Outline each Plasmodium falciparum-infected red blood cell.
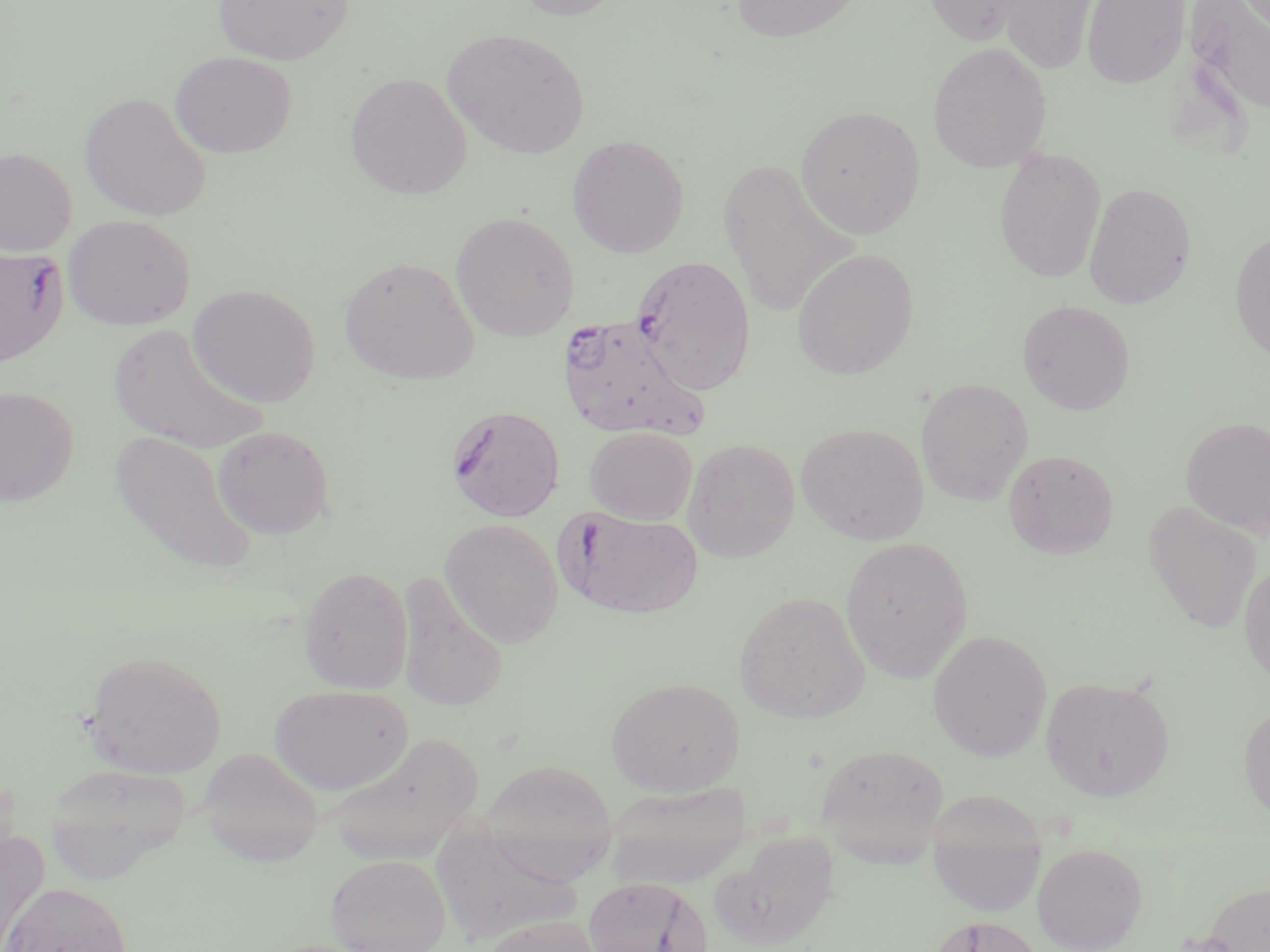

Approximate bounding boxes as named x1/y1/x2/y2 corners in pixels.
Plasmodium falciparum-infected red blood cells: (x1=0, y1=245, x2=68, y2=366), (x1=632, y1=254, x2=756, y2=395), (x1=558, y1=313, x2=710, y2=441), (x1=447, y1=404, x2=566, y2=522), (x1=558, y1=509, x2=705, y2=619).

slide-level diagnosis = Plasmodium falciparum
magnification = 1000x
modality = optical microscopy
stain = May-Grünwald-Giemsa
field of view = single
image size = 1270×952 pixels
preparation = thin blood film
uninfected red blood cell locations = approximate bounding boxes as named x1/y1/x2/y2 corners in pixels: (x1=213, y1=0, x2=354, y2=65), (x1=510, y1=0, x2=627, y2=20), (x1=730, y1=0, x2=861, y2=43), (x1=924, y1=0, x2=1029, y2=46), (x1=1082, y1=0, x2=1191, y2=89), (x1=1182, y1=0, x2=1270, y2=120), (x1=998, y1=1, x2=1099, y2=74), (x1=442, y1=28, x2=590, y2=159), (x1=927, y1=42, x2=1052, y2=173), (x1=169, y1=51, x2=297, y2=158), (x1=345, y1=72, x2=472, y2=199), (x1=79, y1=91, x2=213, y2=222), (x1=795, y1=105, x2=925, y2=239), (x1=567, y1=135, x2=689, y2=258), (x1=0, y1=147, x2=77, y2=256), (x1=994, y1=148, x2=1106, y2=283), (x1=718, y1=156, x2=857, y2=320), (x1=1083, y1=182, x2=1197, y2=309), (x1=450, y1=211, x2=580, y2=342), (x1=63, y1=215, x2=195, y2=330), (x1=1230, y1=229, x2=1270, y2=362), (x1=791, y1=247, x2=919, y2=379), (x1=339, y1=255, x2=480, y2=385), (x1=188, y1=284, x2=321, y2=408), (x1=1017, y1=300, x2=1135, y2=415), (x1=107, y1=323, x2=269, y2=456), (x1=915, y1=377, x2=1034, y2=506), (x1=0, y1=386, x2=79, y2=507), (x1=1181, y1=416, x2=1270, y2=540), (x1=796, y1=422, x2=929, y2=545), (x1=212, y1=424, x2=334, y2=539), (x1=585, y1=426, x2=697, y2=525), (x1=108, y1=428, x2=260, y2=576), (x1=682, y1=438, x2=799, y2=562), (x1=1002, y1=449, x2=1119, y2=559), (x1=1143, y1=499, x2=1262, y2=634), (x1=440, y1=518, x2=563, y2=648), (x1=840, y1=536, x2=973, y2=682), (x1=1239, y1=558, x2=1270, y2=688), (x1=299, y1=565, x2=414, y2=695), (x1=396, y1=571, x2=509, y2=713), (x1=734, y1=590, x2=870, y2=724), (x1=927, y1=630, x2=1052, y2=761), (x1=82, y1=649, x2=226, y2=779), (x1=1040, y1=675, x2=1174, y2=801), (x1=606, y1=676, x2=744, y2=796), (x1=268, y1=684, x2=413, y2=795), (x1=1238, y1=703, x2=1270, y2=824), (x1=321, y1=731, x2=485, y2=866), (x1=815, y1=742, x2=949, y2=866), (x1=208, y1=754, x2=332, y2=864), (x1=479, y1=759, x2=618, y2=883), (x1=43, y1=762, x2=192, y2=883), (x1=605, y1=781, x2=751, y2=889), (x1=928, y1=791, x2=1048, y2=918), (x1=428, y1=821, x2=582, y2=948), (x1=712, y1=831, x2=841, y2=950), (x1=0, y1=832, x2=49, y2=950), (x1=1032, y1=841, x2=1148, y2=952), (x1=325, y1=853, x2=452, y2=952), (x1=583, y1=877, x2=712, y2=952), (x1=1202, y1=880, x2=1270, y2=952), (x1=2, y1=881, x2=132, y2=952), (x1=480, y1=915, x2=603, y2=952), (x1=926, y1=915, x2=1043, y2=952)